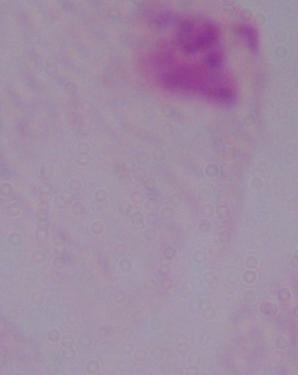
Summary:
  - Magnification: 1000x
  - Identification: trichomonad
  - Modality: photomicrograph